Outline Plasmodium ovale parasites and classify them by life-cycle stage.
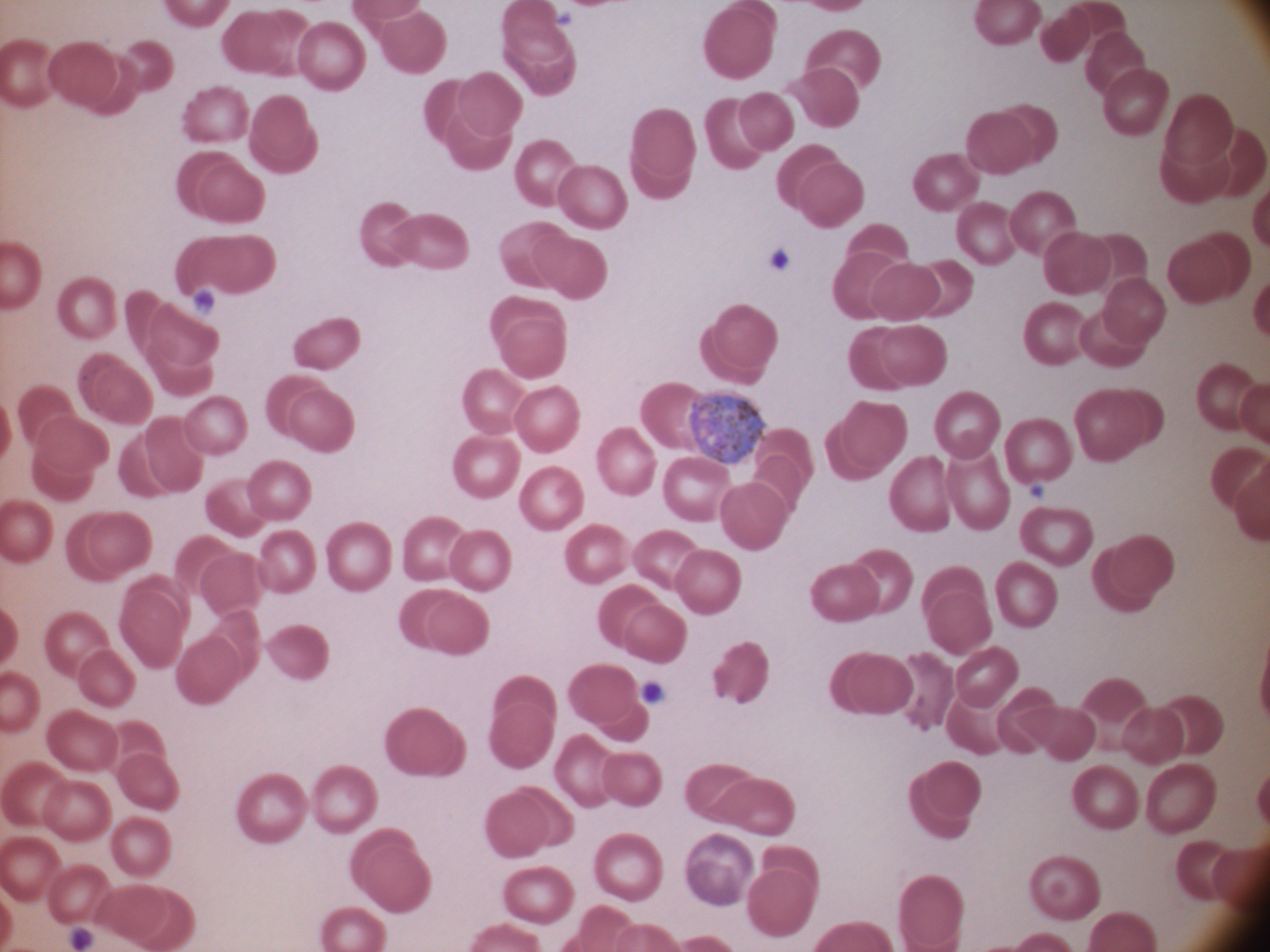

Approximate bounding boxes as [x1, y1, x2, y2] in pixels, from the source annotation, which is not necessarily exhaustive.
Gametocytes: [688, 389, 766, 463].

Single field of view. Giemsa stain. Leica DM2000 optical microscope with a built-in camera. Thin blood smear. Species: Plasmodium ovale. Image is 1270×952 pixels. 100x magnification.